Point out each Plasmodium parasite.
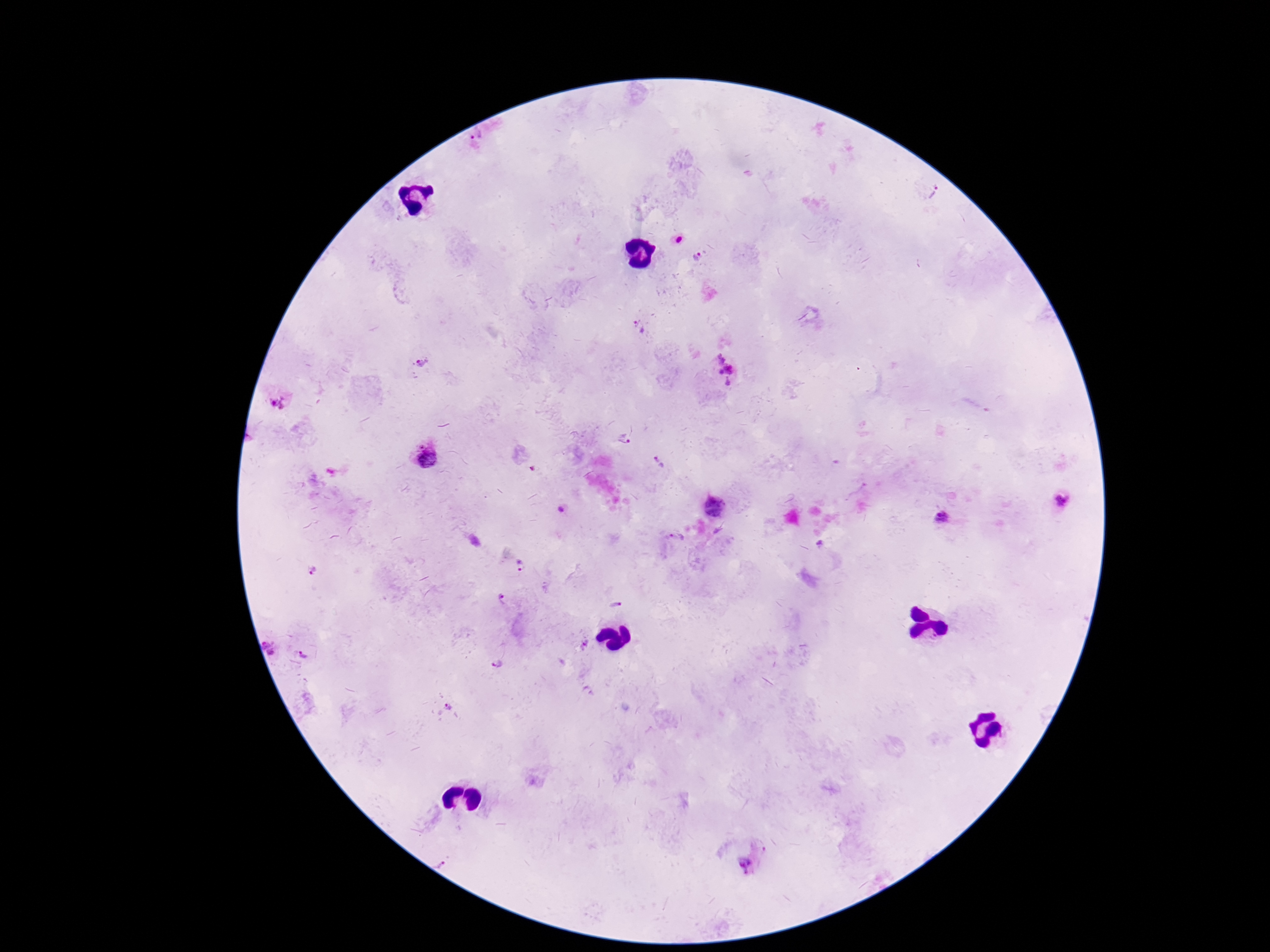
Approximate centers as [x, y] in pixels.
Plasmodium parasites: [478, 134], [936, 194], [680, 240], [697, 256], [638, 326], [720, 358], [422, 363], [729, 368], [721, 372], [728, 382], [278, 401], [623, 439], [421, 445], [428, 459], [659, 463], [1062, 502], [714, 506], [562, 509], [942, 518], [677, 537], [820, 544], [523, 566], [314, 573], [502, 597], [616, 604], [265, 643], [585, 644], [271, 653], [304, 654], [497, 665], [448, 706], [441, 864], [745, 866].

Image is 1270×952 pixels. 100x magnification. Photographed through the microscope eyepiece with a smartphone camera. Thick blood film. Patient malaria status: positive. Single field of view. Giemsa stain.